Identify the parasite.
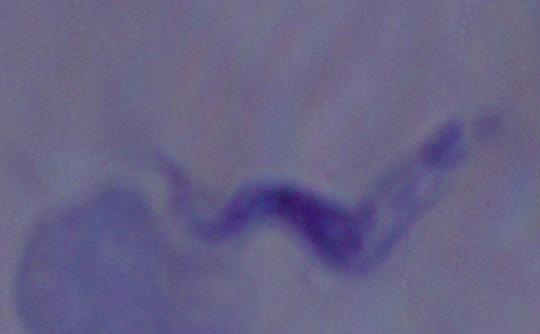
This is a trypanosome.

Summary:
  - Magnification: 1000x
  - Modality: photomicrograph